Name the cell type shown.
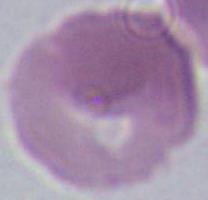

This is an erythrocyte.

Captured at 1000x magnification. Micrograph.